State the preparation type.
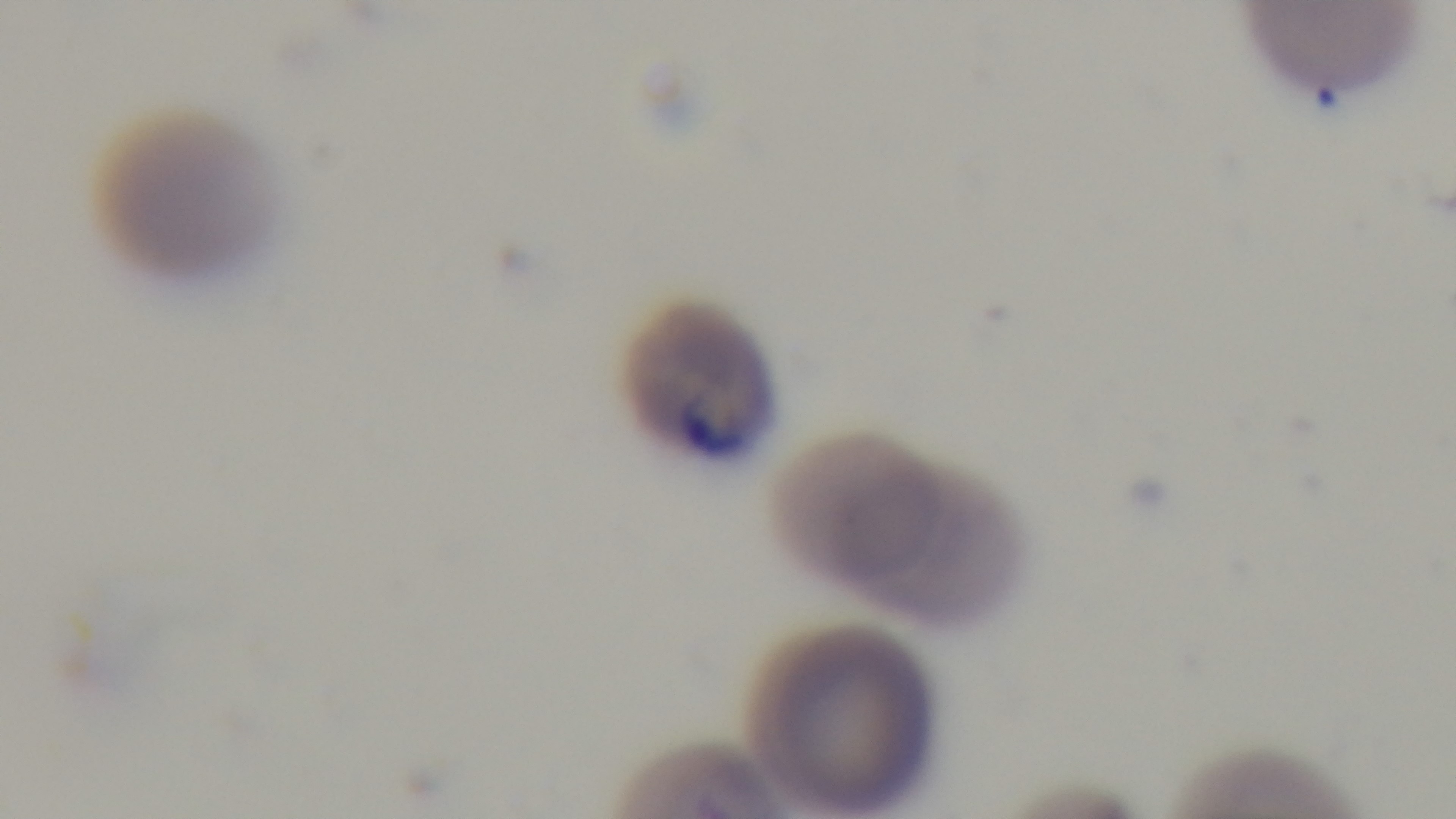

It is a thin blood film.

Malaria status: infected. Photomicrograph. Captured with a mounted 4K digital camera. Single field of view. 100x oil-immersion objective. Giemsa stain.